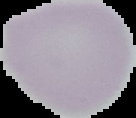

Summary:
  - Preparation: thin blood smear
  - Result: negative for Plasmodium parasites
  - Image size: 136×118 pixels
  - Image type: segmented cell region on a black background